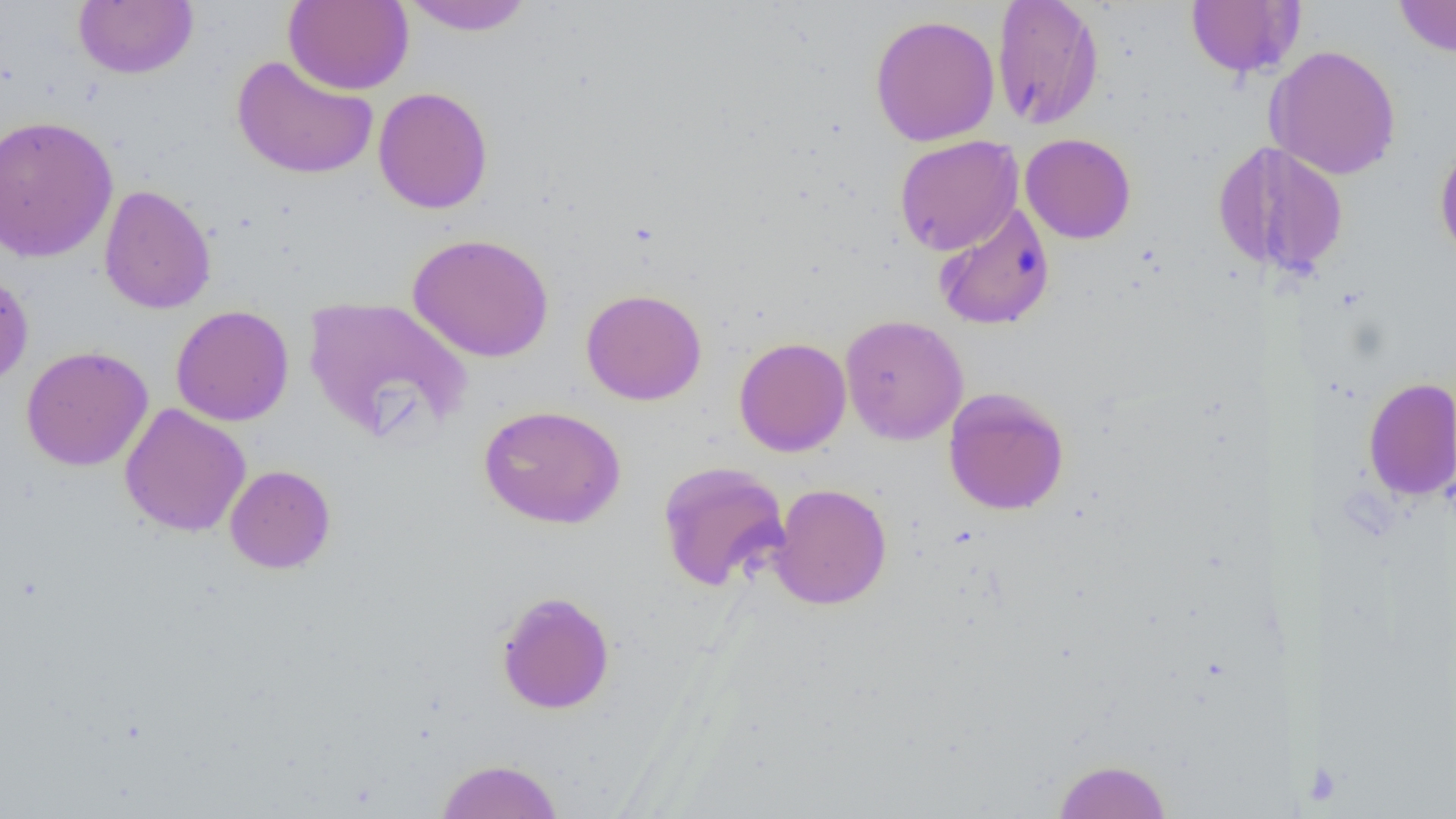
Summary:
  - Coordinate format: approximate bounding boxes as (x1,y1)-(x2,y2) corner pairs in pixels
  - Uninfected red blood cell locations: (283,0)-(414,94), (400,0)-(534,36), (991,0)-(1104,130), (1184,0)-(1299,78), (1394,0)-(1456,57), (74,1)-(198,79), (869,14)-(1001,147), (1267,44)-(1402,180), (231,55)-(379,180), (373,86)-(493,214), (0,114)-(118,263), (1020,133)-(1136,244), (894,135)-(1023,255), (1212,138)-(1261,272), (1434,138)-(1456,262), (1263,142)-(1349,277), (98,184)-(216,315), (932,202)-(1055,331), (407,232)-(555,363), (0,268)-(34,388), (580,288)-(707,406), (302,295)-(473,443), (170,305)-(294,426), (839,314)-(969,445), (733,336)-(851,457), (20,345)-(153,471), (1363,376)-(1456,501), (943,388)-(1070,516), (119,403)-(251,537), (478,403)-(626,529), (656,461)-(791,591), (225,464)-(336,574), (769,482)-(892,610), (496,590)-(615,715), (434,758)-(564,818), (1053,758)-(1172,818)
  - Platelet locations: (1313,758)-(1341,807)
  - Slide-level diagnosis: no evidence of blood parasites
  - Magnification: 1000x
  - Image size: 1456×819 pixels
  - Modality: optical microscopy
  - Field of view: single
  - Preparation: thin blood film